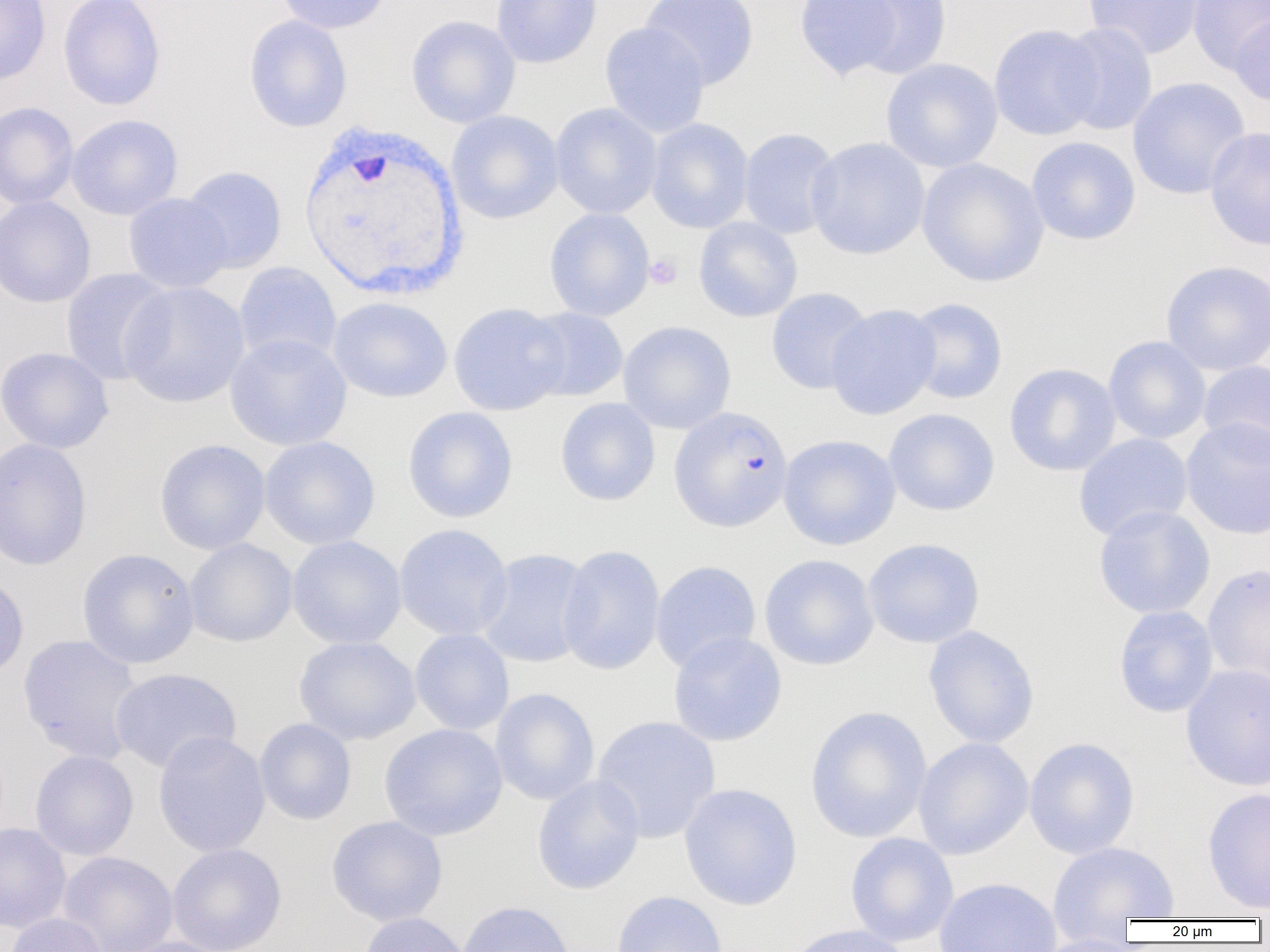
Summary:
  - Coordinate format: approximate bounding boxes as named x1/y1/x2/y2 corners in pixels
  - Platelet locations: (x1=644, y1=253, x2=682, y2=289)
  - Uninfected red blood cell locations: (x1=0, y1=0, x2=51, y2=86), (x1=58, y1=0, x2=166, y2=111), (x1=275, y1=0, x2=391, y2=35), (x1=491, y1=0, x2=602, y2=68), (x1=640, y1=0, x2=759, y2=90), (x1=794, y1=0, x2=905, y2=80), (x1=841, y1=0, x2=953, y2=80), (x1=1083, y1=0, x2=1205, y2=59), (x1=1187, y1=0, x2=1270, y2=75), (x1=1230, y1=12, x2=1270, y2=108), (x1=243, y1=14, x2=352, y2=132), (x1=406, y1=15, x2=521, y2=128), (x1=600, y1=22, x2=710, y2=138), (x1=1056, y1=22, x2=1158, y2=135), (x1=988, y1=24, x2=1105, y2=140), (x1=881, y1=58, x2=1003, y2=173), (x1=1127, y1=77, x2=1250, y2=199), (x1=0, y1=101, x2=79, y2=209), (x1=550, y1=103, x2=662, y2=219), (x1=446, y1=110, x2=564, y2=224), (x1=66, y1=114, x2=183, y2=220), (x1=646, y1=118, x2=754, y2=233), (x1=1204, y1=125, x2=1270, y2=251), (x1=738, y1=128, x2=842, y2=239), (x1=1026, y1=136, x2=1141, y2=245), (x1=806, y1=137, x2=930, y2=260), (x1=916, y1=157, x2=1050, y2=288), (x1=181, y1=166, x2=287, y2=273), (x1=122, y1=193, x2=232, y2=293), (x1=0, y1=196, x2=96, y2=308), (x1=544, y1=208, x2=655, y2=321), (x1=693, y1=217, x2=803, y2=322), (x1=1160, y1=260, x2=1270, y2=375), (x1=233, y1=262, x2=342, y2=366), (x1=60, y1=268, x2=173, y2=385), (x1=119, y1=281, x2=250, y2=408), (x1=766, y1=287, x2=874, y2=394), (x1=327, y1=297, x2=453, y2=402), (x1=904, y1=297, x2=1008, y2=404), (x1=448, y1=302, x2=570, y2=416), (x1=825, y1=304, x2=942, y2=420), (x1=524, y1=307, x2=628, y2=402), (x1=618, y1=320, x2=737, y2=434), (x1=224, y1=333, x2=352, y2=451), (x1=1103, y1=336, x2=1211, y2=444), (x1=0, y1=347, x2=113, y2=454), (x1=1198, y1=360, x2=1270, y2=459), (x1=1004, y1=363, x2=1121, y2=476), (x1=555, y1=398, x2=661, y2=506), (x1=402, y1=406, x2=518, y2=523), (x1=883, y1=408, x2=1000, y2=516), (x1=1180, y1=417, x2=1270, y2=540), (x1=1074, y1=433, x2=1193, y2=541), (x1=778, y1=434, x2=901, y2=550), (x1=259, y1=436, x2=380, y2=549), (x1=0, y1=438, x2=92, y2=571), (x1=154, y1=439, x2=271, y2=554), (x1=1093, y1=505, x2=1215, y2=619), (x1=393, y1=524, x2=513, y2=640), (x1=287, y1=535, x2=407, y2=649), (x1=184, y1=538, x2=297, y2=647), (x1=863, y1=538, x2=985, y2=648), (x1=557, y1=544, x2=665, y2=675), (x1=77, y1=548, x2=199, y2=669), (x1=475, y1=548, x2=594, y2=668), (x1=759, y1=554, x2=880, y2=671), (x1=650, y1=561, x2=761, y2=672), (x1=1202, y1=563, x2=1270, y2=687), (x1=0, y1=573, x2=28, y2=684), (x1=1113, y1=605, x2=1219, y2=718), (x1=923, y1=625, x2=1040, y2=748), (x1=409, y1=628, x2=514, y2=735), (x1=668, y1=631, x2=787, y2=747), (x1=17, y1=634, x2=143, y2=764), (x1=293, y1=636, x2=421, y2=745), (x1=1181, y1=664, x2=1270, y2=791), (x1=109, y1=668, x2=242, y2=773), (x1=490, y1=688, x2=600, y2=806), (x1=805, y1=705, x2=932, y2=843), (x1=591, y1=716, x2=721, y2=843), (x1=255, y1=718, x2=357, y2=825), (x1=378, y1=723, x2=508, y2=842), (x1=152, y1=731, x2=271, y2=857), (x1=1024, y1=736, x2=1140, y2=859), (x1=913, y1=737, x2=1034, y2=859), (x1=29, y1=750, x2=139, y2=860), (x1=532, y1=775, x2=645, y2=895), (x1=678, y1=783, x2=803, y2=911), (x1=1201, y1=787, x2=1270, y2=914), (x1=326, y1=816, x2=448, y2=926), (x1=0, y1=822, x2=71, y2=934), (x1=845, y1=832, x2=959, y2=947), (x1=1048, y1=841, x2=1179, y2=924), (x1=167, y1=844, x2=287, y2=952), (x1=57, y1=851, x2=178, y2=952), (x1=933, y1=876, x2=1062, y2=952), (x1=611, y1=890, x2=727, y2=952), (x1=456, y1=900, x2=576, y2=952), (x1=4, y1=913, x2=108, y2=952), (x1=358, y1=913, x2=471, y2=952), (x1=784, y1=923, x2=913, y2=952), (x1=1030, y1=934, x2=1143, y2=952), (x1=115, y1=936, x2=239, y2=952)
  - Plasmodium falciparum-infected red blood cell locations: (x1=669, y1=405, x2=793, y2=532)
  - White blood cell locations: (x1=296, y1=116, x2=470, y2=303)
  - Slide-level diagnosis: Plasmodium falciparum
  - Field of view: single
  - Preparation: thin blood film
  - Image size: 1270×952 pixels
  - Magnification: 1000x
  - Modality: light microscopy